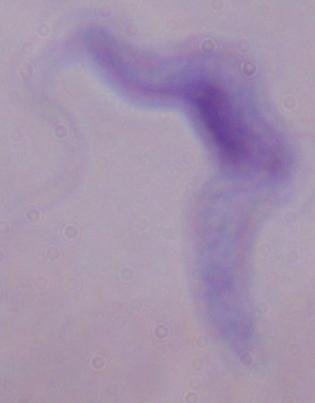
{
  "magnification": "1000x",
  "identification": "trypanosome",
  "modality": "photomicrograph"
}